Report the malaria status of this cell.
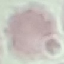
It is uninfected.

Summary:
  - Image type: cell patch, automatically extracted from a larger field of view and resized to 64 × 64 pixels
  - Capture: smartphone camera at the microscope eyepiece
  - Stain: Giemsa
  - Preparation: thin blood film